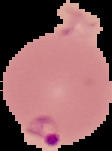 Segmented cell region on a black background. Image is 112×151 pixels. Malaria status: parasitized. From a thin blood film.